Point out each malaria parasite and each leukocyte.
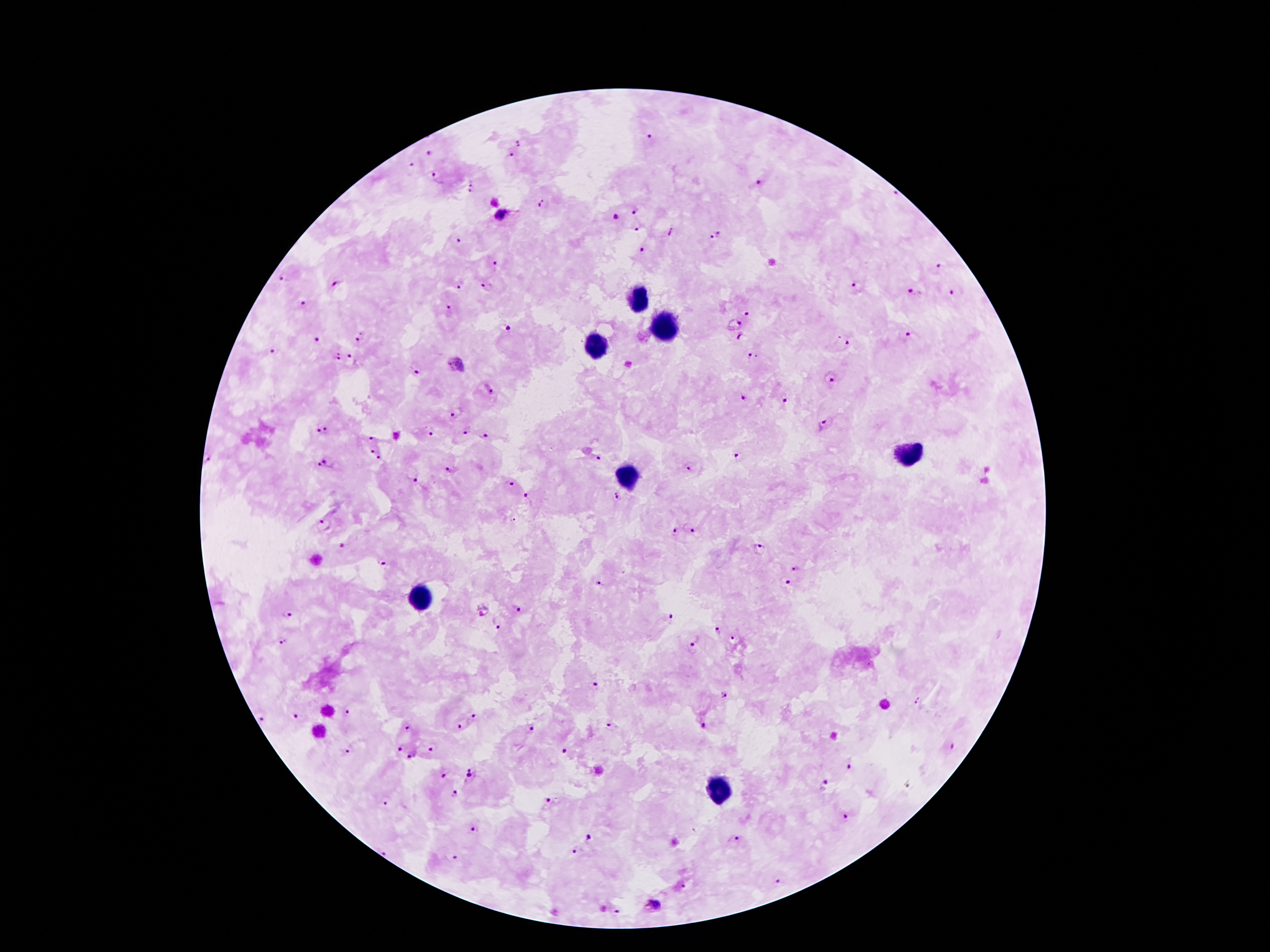

Approximate object centers, in pixels from the top-left corner.
Malaria parasites: (x=650, y=138), (x=519, y=143), (x=430, y=153), (x=510, y=154), (x=412, y=163), (x=438, y=176), (x=757, y=182), (x=471, y=187), (x=545, y=205), (x=635, y=210), (x=500, y=215), (x=616, y=217), (x=637, y=230), (x=671, y=232), (x=716, y=235), (x=458, y=240), (x=642, y=251), (x=495, y=261), (x=941, y=269), (x=284, y=279), (x=334, y=283), (x=487, y=285), (x=458, y=287), (x=857, y=287), (x=912, y=293), (x=950, y=293), (x=306, y=303), (x=448, y=308), (x=746, y=313), (x=734, y=323), (x=508, y=327), (x=361, y=336), (x=742, y=337), (x=907, y=337), (x=316, y=341), (x=846, y=345), (x=275, y=349), (x=338, y=356), (x=351, y=356), (x=752, y=359), (x=415, y=369), (x=829, y=380), (x=494, y=391), (x=744, y=397), (x=783, y=397), (x=457, y=411), (x=824, y=424), (x=468, y=430), (x=323, y=431), (x=430, y=432), (x=485, y=437), (x=372, y=438), (x=371, y=450), (x=600, y=457), (x=740, y=457), (x=379, y=460), (x=209, y=461), (x=322, y=465), (x=689, y=467), (x=448, y=470), (x=412, y=478), (x=511, y=482), (x=526, y=497), (x=617, y=497), (x=324, y=525), (x=675, y=530), (x=695, y=532), (x=345, y=546), (x=759, y=549), (x=381, y=563), (x=796, y=566), (x=786, y=582), (x=600, y=583), (x=482, y=611), (x=518, y=611), (x=289, y=615), (x=669, y=617), (x=496, y=626), (x=717, y=630), (x=733, y=638), (x=282, y=641), (x=693, y=641), (x=594, y=686), (x=723, y=695), (x=918, y=701), (x=346, y=713), (x=295, y=714), (x=475, y=715), (x=265, y=720), (x=702, y=725), (x=459, y=726), (x=609, y=726), (x=404, y=727), (x=530, y=727), (x=953, y=746), (x=400, y=748), (x=434, y=748), (x=349, y=749), (x=566, y=751), (x=412, y=755), (x=851, y=767), (x=443, y=776), (x=471, y=776), (x=823, y=785), (x=908, y=787), (x=456, y=793), (x=384, y=804), (x=549, y=804), (x=847, y=817), (x=475, y=828), (x=590, y=837), (x=735, y=839), (x=575, y=850), (x=383, y=852), (x=457, y=858), (x=779, y=882), (x=685, y=886), (x=616, y=913).
Leukocytes: (x=638, y=300), (x=665, y=327), (x=599, y=347), (x=905, y=455), (x=627, y=477), (x=419, y=599), (x=720, y=792).

{
  "patient_malaria_status": "positive for Plasmodium falciparum",
  "capture": "smartphone through the microscope eyepiece",
  "image_size": "1270×952 pixels",
  "magnification": "100x",
  "preparation": "thick blood film",
  "field_of_view": "one from this slide",
  "stain": "Giemsa"
}